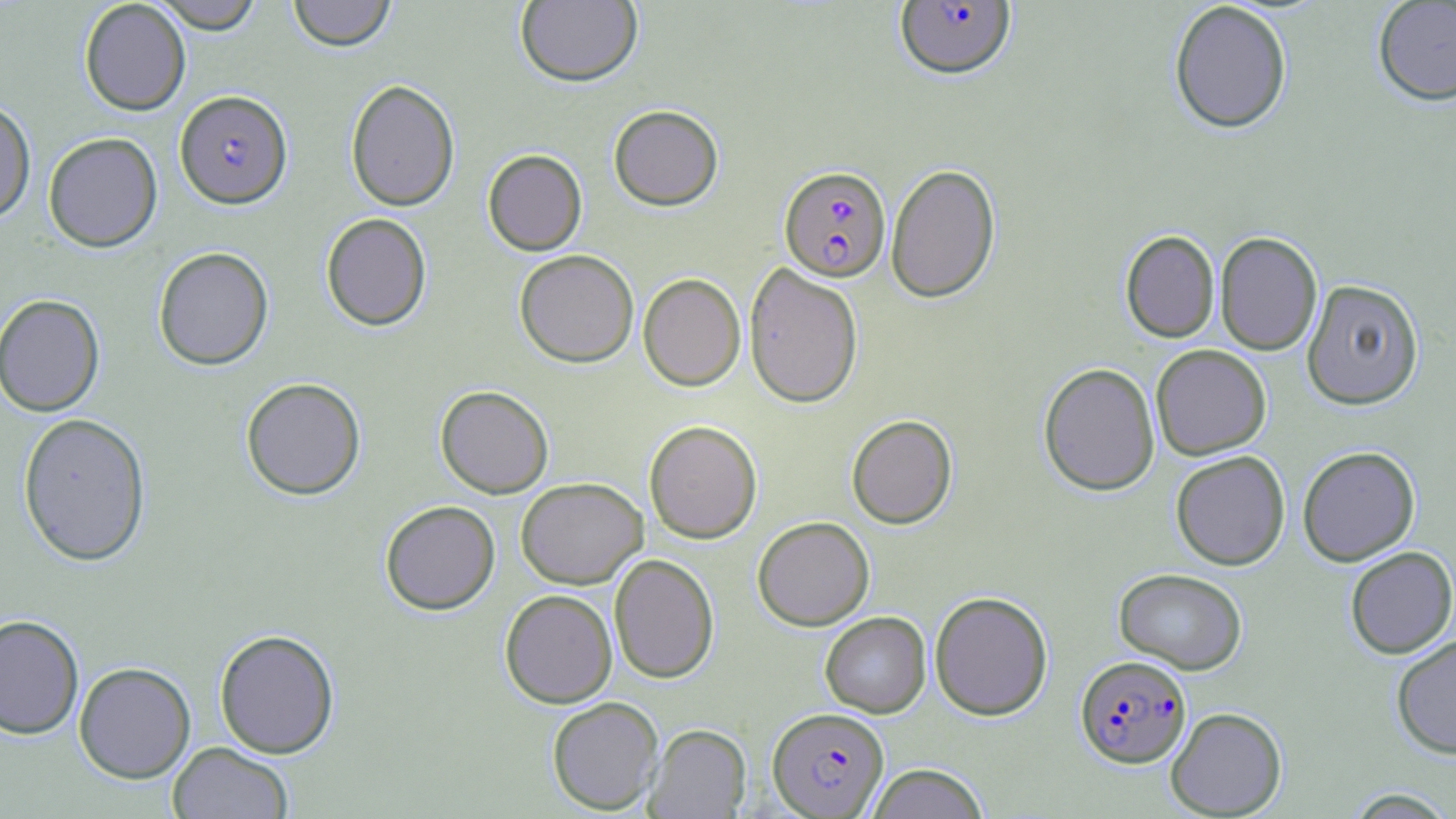

Summary:
  - Coordinate format: approximate bounding boxes as [x1, y1, x2, y2] in pixels
  - Plasmodium falciparum-infected red blood cell locations: [894, 2, 1016, 81], [175, 90, 292, 208], [779, 165, 891, 282], [1075, 655, 1191, 768], [767, 707, 889, 817]
  - Uninfected red blood cell locations: [78, 0, 191, 115], [150, 0, 265, 33], [288, 0, 396, 51], [515, 0, 642, 87], [1372, 0, 1456, 106], [1168, 1, 1293, 134], [345, 79, 460, 211], [0, 97, 36, 224], [608, 104, 723, 211], [43, 132, 163, 252], [483, 149, 587, 256], [886, 163, 1001, 303], [321, 213, 431, 331], [1120, 230, 1219, 343], [1215, 231, 1322, 355], [153, 246, 274, 370], [514, 249, 639, 368], [744, 262, 863, 408], [638, 273, 745, 391], [1301, 278, 1424, 409], [0, 294, 105, 416], [1151, 344, 1271, 460], [1038, 362, 1160, 496], [241, 377, 366, 500], [435, 385, 554, 498], [17, 412, 152, 566], [846, 414, 958, 529], [644, 420, 762, 543], [1298, 446, 1420, 565], [1170, 451, 1290, 570], [516, 477, 647, 589], [380, 500, 500, 615], [752, 516, 875, 631], [1344, 546, 1456, 658], [609, 553, 719, 684], [1113, 568, 1248, 674], [499, 589, 617, 708], [929, 591, 1053, 721], [820, 611, 931, 718], [0, 614, 84, 740], [214, 628, 340, 759], [1391, 633, 1456, 759], [74, 662, 196, 783], [547, 696, 664, 815], [1165, 706, 1287, 817], [644, 723, 751, 818], [168, 741, 294, 819], [867, 763, 989, 819], [1339, 786, 1456, 817]
  - Slide-level diagnosis: Plasmodium falciparum
  - Image size: 1456×819 pixels
  - Modality: optical microscopy
  - Magnification: 1000x
  - Stain: May-Grünwald-Giemsa
  - Field of view: single
  - Preparation: thin blood smear